Name the blood parasite species.
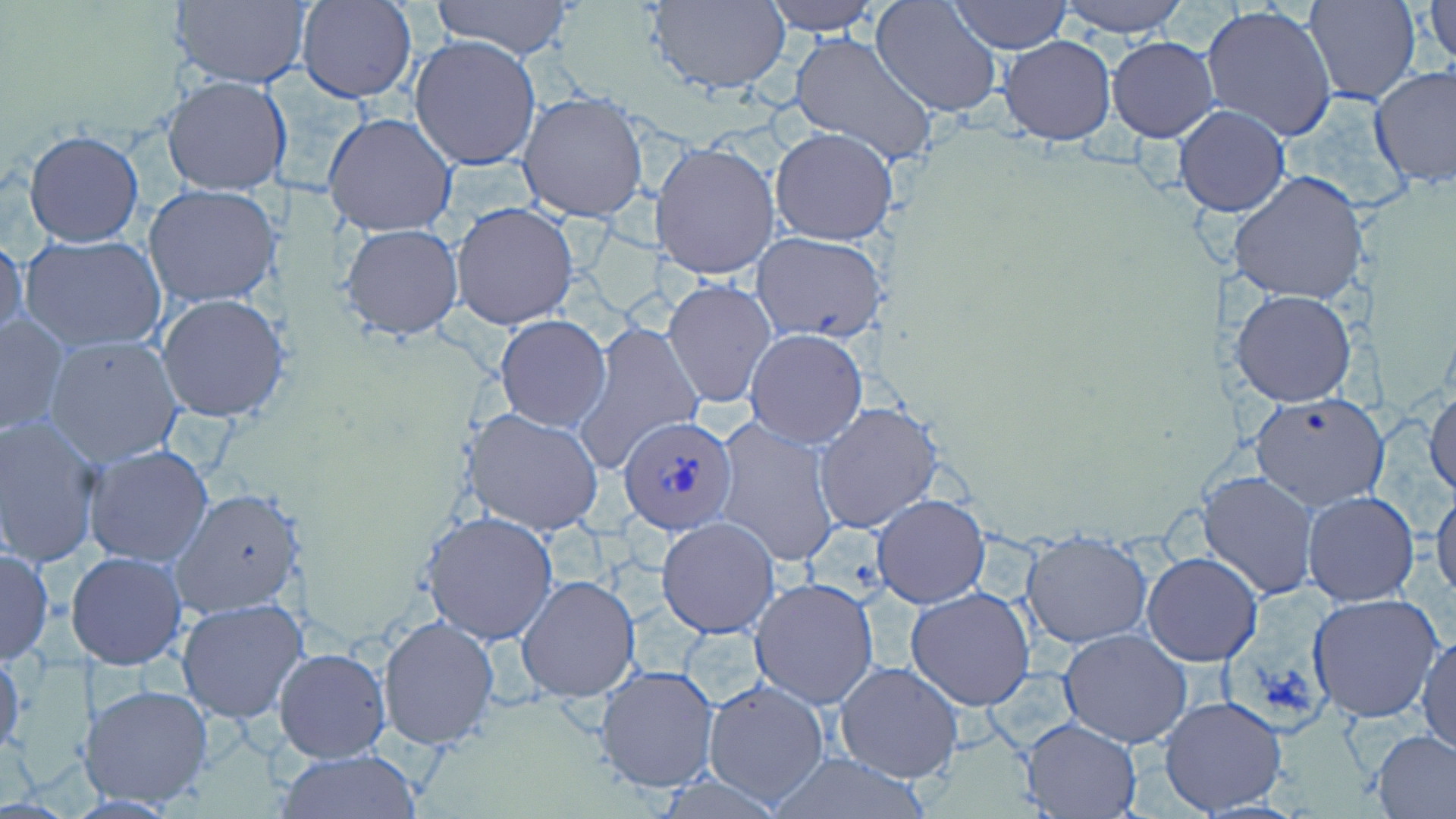
Plasmodium ovale.

preparation = thin blood smear
Plasmodium ovale-infected red blood cell locations = approximate bounding boxes as (x1, y1, x2, y2) in pixels: (617, 412, 739, 534)
stain = May-Grünwald-Giemsa
modality = light microscopy
magnification = 1000x
uninfected red blood cell locations = approximate bounding boxes as (x1, y1, x2, y2) in pixels: (297, 0, 417, 102), (428, 0, 575, 61), (762, 0, 882, 36), (949, 0, 1071, 52), (1054, 0, 1190, 36), (1302, 0, 1420, 105), (169, 1, 311, 88), (646, 1, 792, 94), (871, 1, 1004, 118), (1425, 1, 1455, 68), (1200, 4, 1339, 143), (788, 31, 939, 168), (409, 35, 541, 170), (998, 35, 1116, 145), (1106, 36, 1219, 143), (1369, 65, 1456, 188), (161, 75, 292, 196), (517, 90, 649, 222), (1175, 104, 1291, 216), (321, 112, 458, 239), (769, 127, 897, 246), (23, 130, 144, 247), (651, 140, 781, 281), (1230, 169, 1369, 308), (143, 184, 283, 307), (450, 201, 579, 330), (339, 223, 465, 342), (751, 232, 887, 344), (0, 234, 28, 350), (22, 236, 167, 352), (664, 278, 776, 408), (1232, 290, 1356, 407), (155, 294, 288, 423), (0, 313, 69, 437), (495, 315, 612, 430), (575, 320, 705, 474), (744, 327, 868, 449), (43, 334, 186, 466), (1426, 388, 1456, 501), (1249, 392, 1389, 510), (813, 399, 945, 535), (462, 408, 606, 535), (0, 414, 104, 568), (711, 419, 842, 567), (83, 444, 215, 567), (1199, 470, 1320, 601), (1431, 487, 1456, 605), (172, 488, 305, 618), (1302, 492, 1419, 606), (872, 494, 991, 608), (420, 510, 561, 645), (657, 516, 780, 637), (1021, 530, 1152, 647), (0, 547, 53, 665), (67, 551, 188, 671), (1142, 552, 1263, 666), (515, 574, 639, 703), (749, 575, 880, 709), (904, 587, 1037, 711), (1306, 593, 1446, 724), (176, 597, 309, 723), (377, 614, 500, 749), (1059, 628, 1192, 748), (1417, 629, 1455, 757), (0, 646, 26, 762), (275, 646, 391, 763), (834, 660, 965, 784), (594, 664, 720, 793), (702, 678, 831, 807), (81, 683, 215, 810), (1157, 694, 1289, 816), (1019, 718, 1142, 817), (1370, 729, 1456, 819), (278, 748, 420, 817), (770, 749, 931, 818)
field of view = one of a larger specimen
image size = 1456×819 pixels